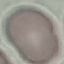

Summary:
  - Malaria status: uninfected
  - Image type: automatically extracted cell patch, resized to 64 × 64 pixels
  - Preparation: thin blood smear
  - Stain: Giemsa
  - Capture: smartphone camera at the microscope eyepiece